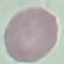
malaria_status: uninfected
stain: Giemsa
capture: smartphone through the microscope eyepiece
preparation: thin blood film
image_type: cell patch, automatically extracted from a larger field of view and resized to 64 × 64 pixels